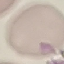
malaria status = uninfected
image type = cell patch, automatically extracted from a larger field of view and resized to 64 × 64 pixels
capture = smartphone camera at the microscope eyepiece
preparation = thin blood film
stain = Giemsa